Assess this cell for malaria.
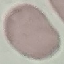

Uninfected.

Summary:
  - Capture: smartphone camera at the microscope eyepiece
  - Image type: automatically extracted cell patch, resized to 64 × 64 pixels
  - Preparation: thin blood smear
  - Stain: Giemsa